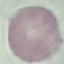

result = no malaria parasites seen
preparation = thin blood smear
capture = smartphone through the microscope eyepiece
image type = cell patch, automatically extracted from a larger field of view and resized to 64 × 64 pixels
stain = Giemsa